Look for parasitized red blood cells.
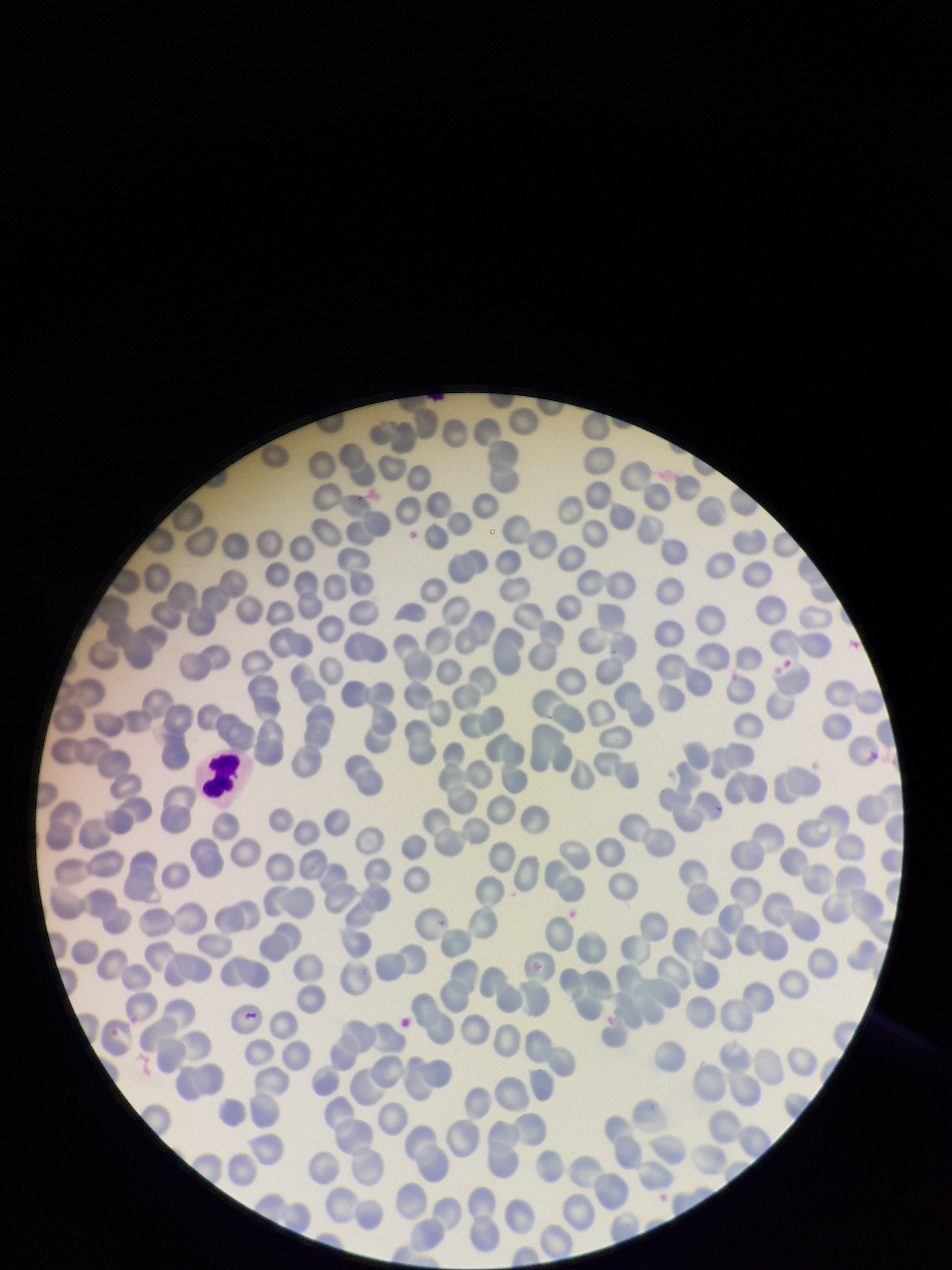
None detected.

{
  "image_size": "952×1270 pixels",
  "patient_malaria_status": "negative",
  "preparation": "thin",
  "parasitized_red_blood_cell_count": 0,
  "capture": "smartphone photograph through the microscope eyepiece",
  "field_of_view": "one from this slide",
  "red_blood_cell_count": 233,
  "stain": "Giemsa"
}